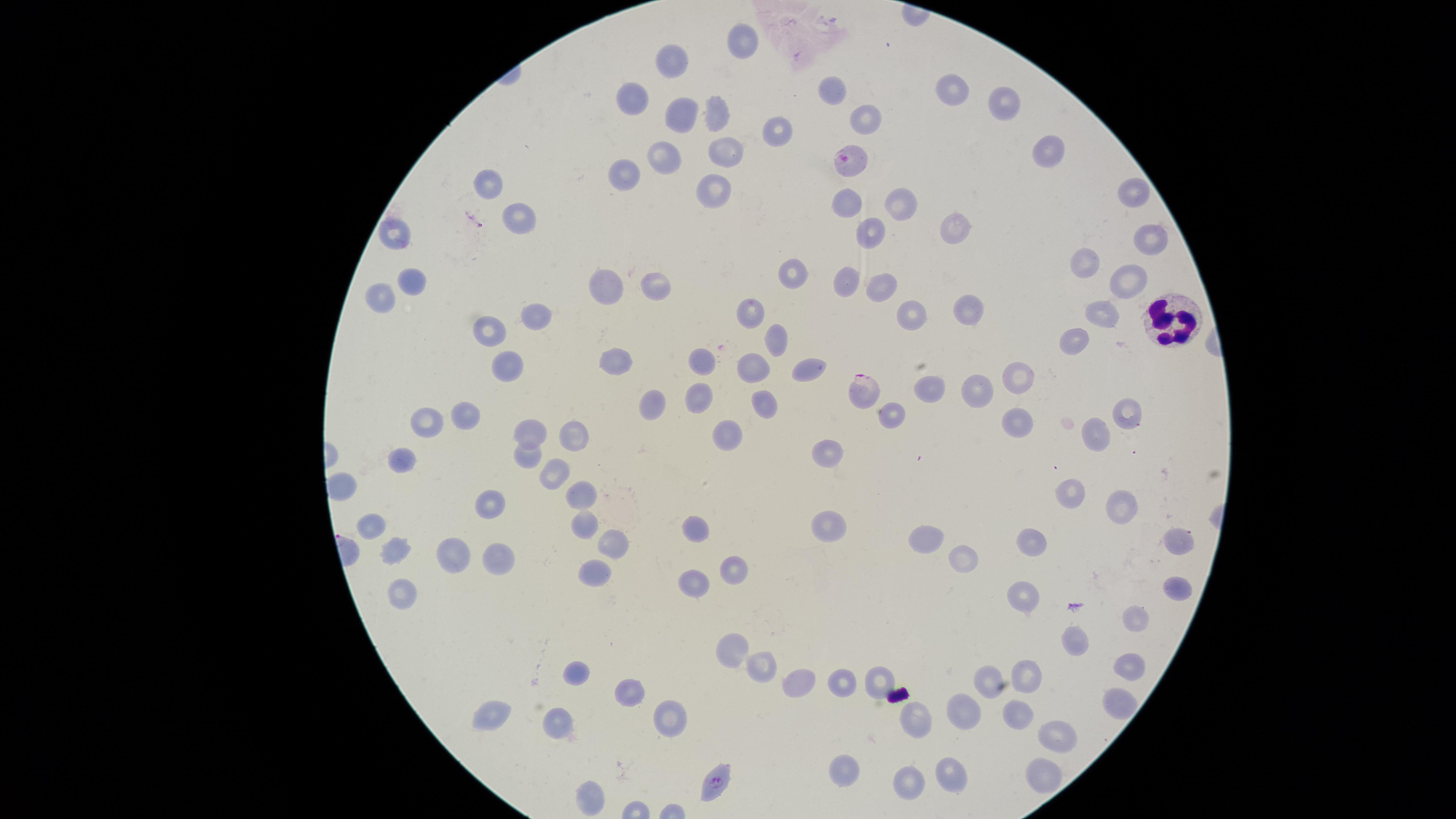
{
  "uninfected_red_blood_cells": "approximate marker points as (x, y) in pixels: (744, 41), (675, 61), (833, 94), (948, 97), (637, 99), (1000, 107), (680, 111), (715, 111), (870, 111), (774, 129), (723, 148), (1046, 148), (663, 153), (631, 174), (712, 186), (494, 189), (1130, 191), (846, 201), (895, 206), (523, 221), (950, 223), (879, 229), (1152, 232), (395, 234), (1088, 262), (798, 272), (412, 276), (843, 279), (1129, 280), (607, 284), (656, 284), (882, 287), (384, 292), (753, 307), (968, 309), (1103, 313), (535, 316), (914, 317), (488, 328), (775, 333), (1077, 337), (618, 356), (694, 356), (757, 365), (506, 366), (804, 368), (1023, 374), (978, 386), (924, 387), (694, 389), (766, 401), (654, 408), (889, 410), (1125, 412), (464, 413), (428, 417), (1005, 422), (733, 432), (530, 434), (1098, 434), (577, 437), (830, 447), (529, 457), (404, 458), (558, 476), (344, 481), (1074, 493), (577, 494), (1121, 504), (483, 505), (373, 523), (584, 523), (825, 528), (697, 529), (923, 537), (1177, 537), (610, 541), (1035, 544), (395, 552), (495, 554), (455, 555), (967, 559), (736, 567), (593, 575), (693, 584), (1175, 584), (400, 590), (1027, 595), (1133, 620), (1080, 635), (728, 646), (757, 665), (1025, 668), (1128, 668), (573, 672), (794, 676), (840, 676), (877, 677), (990, 679), (631, 687), (1113, 700), (485, 710), (969, 710), (1018, 712), (918, 715), (673, 720), (557, 722), (1061, 732), (849, 769), (1041, 769), (948, 774), (909, 777), (596, 798)",
  "visible_region": "circular",
  "preparation": "thin blood film",
  "stain": "Giemsa",
  "presence": "malaria parasites detected",
  "capture": "smartphone photograph through the microscope eyepiece",
  "parasitized_red_blood_cells": "approximate marker points as (x, y) in pixels: (850, 161), (859, 391), (715, 784)",
  "image_size": "1456×819 pixels",
  "field_of_view": "single",
  "species": "Plasmodium falciparum",
  "white_blood_cells": "approximate marker points as (x, y) in pixels: (1179, 321)"
}